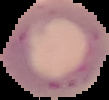
Image is 109×100 pixels. Result: negative for Plasmodium parasites. From a thin blood smear. The area outside the segmented cell region is set to black.